Comment on the morphology of the erythrocytes.
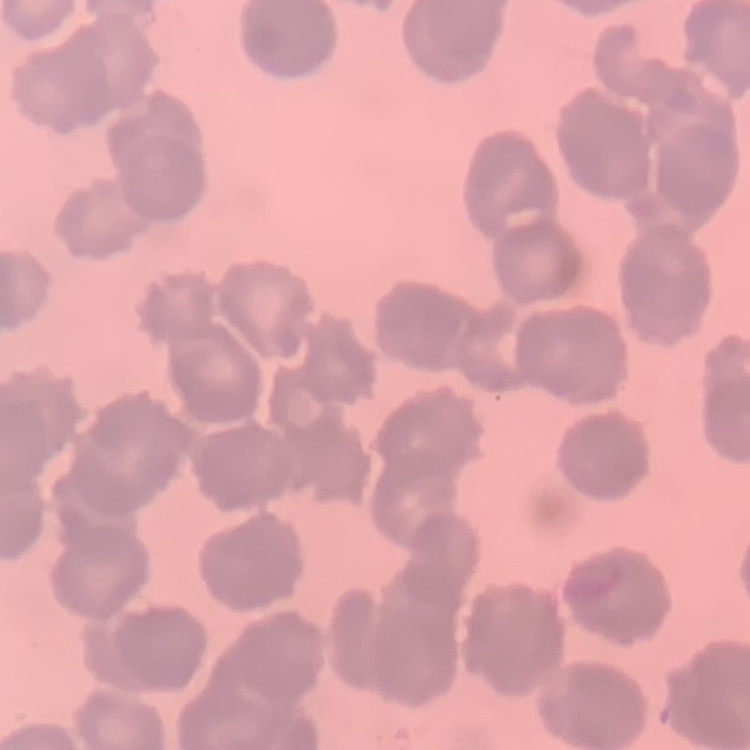
They show rouleaux formation.

Summary:
  - Stain: Field's or Giemsa
  - Image type: one tile cut from a larger photomicrograph
  - Preparation: thin blood smear